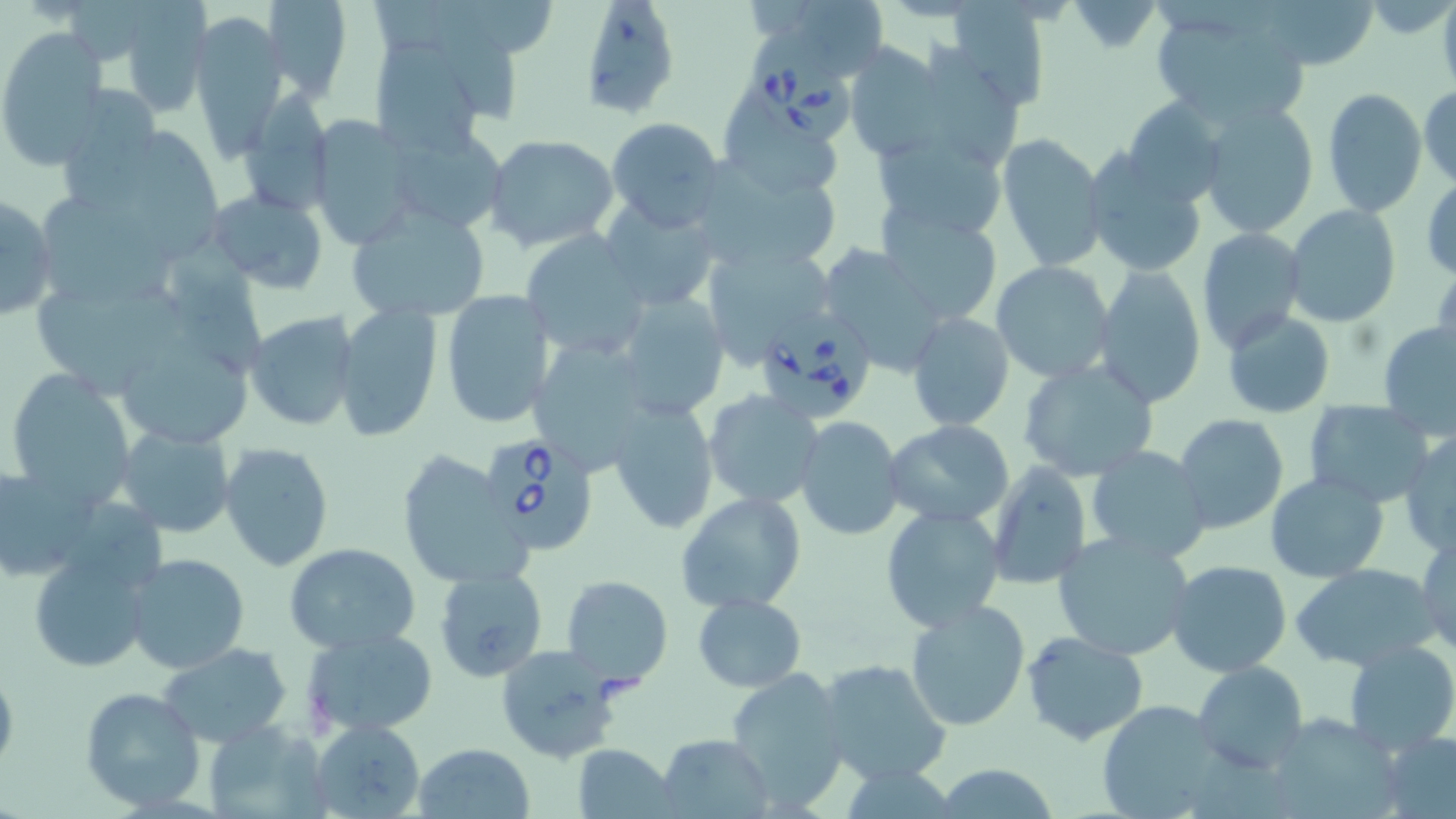

slide-level diagnosis = Babesia divergens
modality = light microscopy
magnification = 1000x
image size = 1456×819 pixels
preparation = thin blood smear
field of view = one of a larger specimen
stain = May-Grünwald-Giemsa
Babesia divergens-infected red blood cell locations = approximate bounding boxes as (x1,y1)-(x2,y2) corner pairs in pixels: (748,30)-(858,145), (756,308)-(883,424), (480,434)-(598,552)
uninfected red blood cell locations = approximate bounding boxes as (x1,y1)-(x2,y2) corner pairs in pixels: (260,0)-(353,102), (381,0)-(516,117), (576,0)-(681,122), (939,0)-(1052,109), (1259,0)-(1379,71), (118,1)-(212,119), (1066,1)-(1161,52), (1146,7)-(1314,128), (191,14)-(286,155), (0,29)-(110,164), (920,35)-(1026,161), (365,36)-(499,159), (843,40)-(946,160), (1418,82)-(1455,188), (62,84)-(164,217), (1320,87)-(1427,217), (241,91)-(331,218), (728,96)-(838,201), (1121,97)-(1231,210), (1199,101)-(1318,237), (307,114)-(421,250), (605,118)-(726,230), (386,124)-(511,235), (873,129)-(1005,242), (137,132)-(232,262), (483,133)-(619,252), (996,133)-(1109,272), (1083,151)-(1207,278), (686,153)-(846,273), (1424,176)-(1456,280), (206,188)-(331,293), (1,192)-(59,322), (45,195)-(184,308), (599,199)-(721,310), (1284,204)-(1401,329), (347,205)-(491,322), (879,205)-(1005,327), (1196,227)-(1306,354), (522,230)-(650,359), (164,231)-(266,395), (703,245)-(838,364), (816,245)-(949,375), (991,261)-(1115,382), (1093,265)-(1207,408), (30,285)-(187,396), (613,288)-(730,420), (439,289)-(555,430), (334,304)-(442,442), (1222,309)-(1335,419), (243,310)-(361,432), (906,310)-(1016,433), (1378,321)-(1456,439), (527,337)-(663,475), (125,339)-(258,445), (1016,359)-(1161,484), (5,367)-(136,505), (700,388)-(826,512), (608,397)-(717,533), (1304,401)-(1434,507), (1173,413)-(1288,534), (793,416)-(905,539), (883,421)-(1015,528), (114,424)-(236,538), (1399,433)-(1455,557), (220,443)-(336,573), (1085,446)-(1212,564), (395,450)-(525,588), (988,462)-(1093,588), (1,467)-(90,587), (1265,473)-(1390,583), (676,491)-(806,613), (880,506)-(1006,632), (1416,530)-(1456,658), (1052,531)-(1195,661), (284,542)-(421,654), (28,549)-(155,673), (124,553)-(251,675), (1165,561)-(1294,678), (1294,564)-(1440,671), (434,566)-(551,683), (560,576)-(673,688), (693,593)-(805,691), (905,598)-(1032,732), (304,626)-(440,735), (1021,632)-(1150,746), (1342,640)-(1456,752), (158,642)-(294,747), (494,644)-(627,764), (819,656)-(953,787), (1192,661)-(1307,774), (724,667)-(849,810), (78,687)-(205,811), (1096,700)-(1233,818), (1297,708)-(1408,819), (308,718)-(427,818), (203,721)-(328,818), (1381,730)-(1456,819), (657,732)-(774,818), (412,743)-(535,819), (573,743)-(677,819), (930,763)-(1061,819)